Assess this cell for malaria.
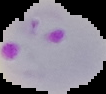

Parasitized.

image type = segmented cell region with the area outside set to black
preparation = thin blood smear
image size = 106×94 pixels